Locate every Plasmodium malariae-infected red blood cell.
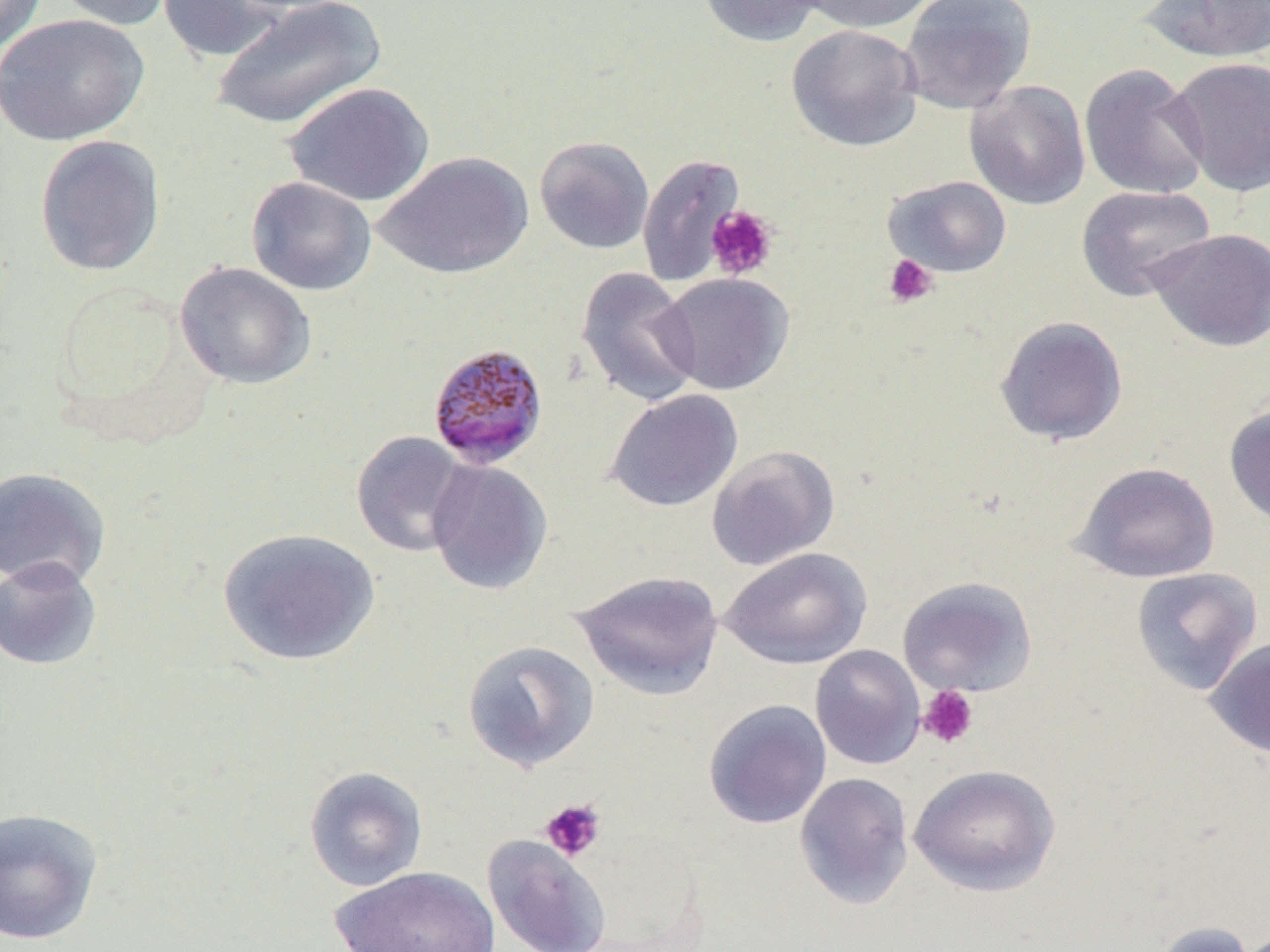

Approximate bounding boxes as [x1, y1, x2, y2] in pixels.
Plasmodium malariae-infected red blood cells: [427, 342, 549, 470].

Platelet locations: [706, 205, 779, 280], [883, 254, 939, 308], [917, 684, 979, 749], [539, 798, 606, 862]. Uninfected red blood cell locations: [0, 0, 47, 54], [52, 0, 178, 32], [157, 0, 289, 63], [210, 0, 387, 131], [697, 0, 827, 47], [797, 0, 940, 34], [899, 0, 1037, 115], [1138, 0, 1270, 64], [1, 13, 149, 146], [786, 23, 924, 152], [1166, 56, 1270, 197], [1079, 63, 1210, 201], [964, 80, 1091, 210], [283, 82, 435, 207], [35, 135, 166, 276], [534, 135, 655, 255], [372, 150, 534, 280], [637, 152, 746, 287], [883, 175, 1012, 277], [246, 176, 377, 296], [1076, 185, 1216, 302], [1146, 228, 1270, 352], [175, 261, 317, 390], [575, 266, 702, 407], [657, 273, 794, 396], [993, 315, 1129, 446], [605, 388, 743, 512], [1223, 404, 1270, 530], [350, 430, 473, 558], [706, 444, 840, 570], [425, 458, 553, 595], [1071, 461, 1221, 583], [0, 466, 111, 591], [217, 527, 380, 666], [720, 547, 872, 669], [0, 556, 103, 672], [1131, 566, 1263, 696], [571, 569, 725, 701], [897, 575, 1038, 697], [1205, 638, 1270, 759], [461, 639, 600, 773], [810, 644, 925, 770], [703, 699, 832, 829], [908, 763, 1060, 897], [303, 765, 429, 891], [794, 772, 914, 910], [0, 807, 104, 945], [482, 835, 611, 952], [330, 865, 501, 952], [1150, 921, 1258, 952]. Slide-level diagnosis: Plasmodium malariae. Thin blood film. Single field of view. Light microscopy. Image is 1270×952 pixels. Captured at 1000x magnification.